Assess this cell for malaria.
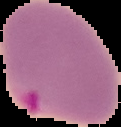
It is parasitized.

image_type: segmented cell region with the area outside set to black
preparation: thin blood film
image_size: 121×127 pixels